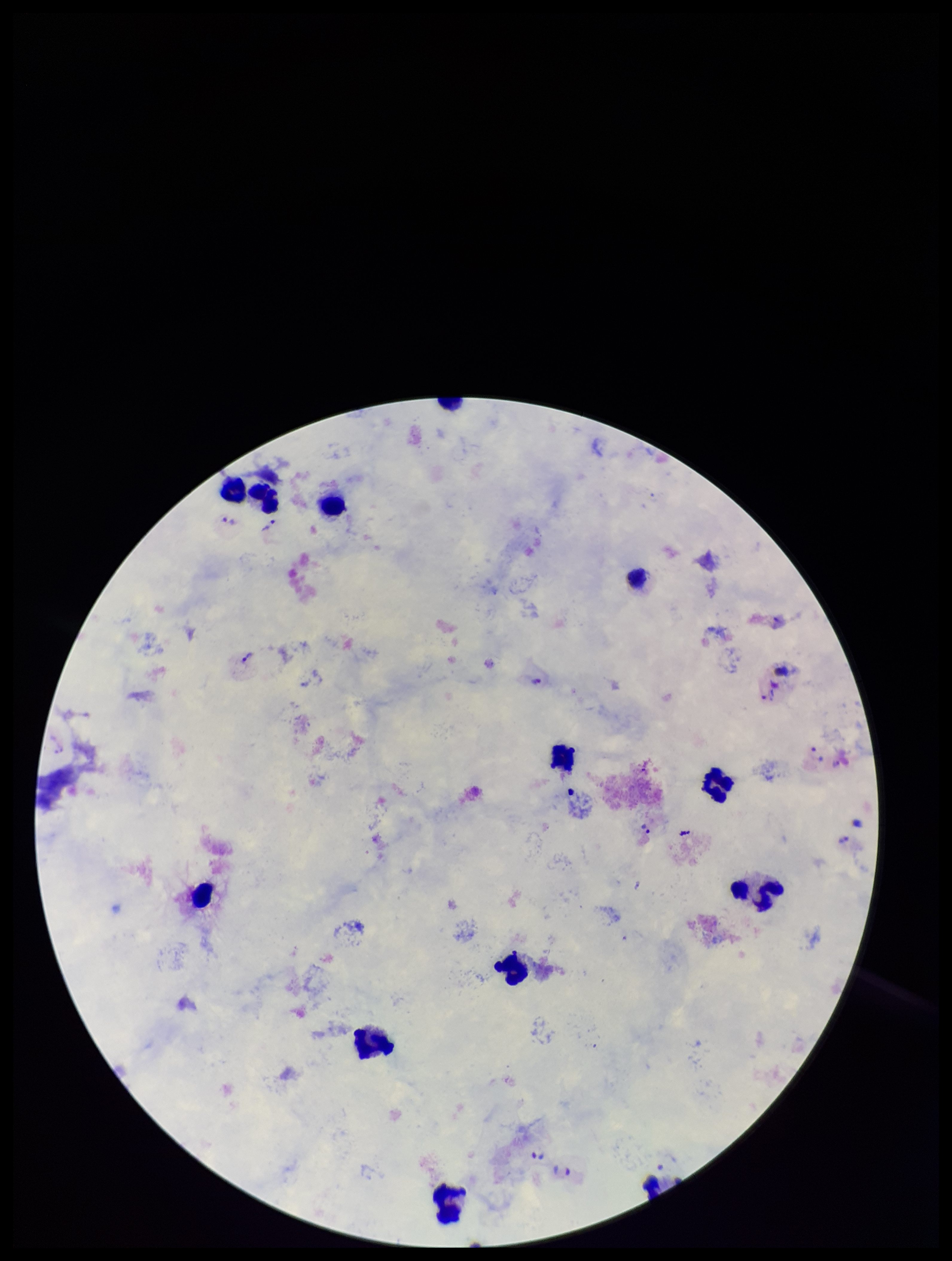
Summary:
  - Preparation: thick smear
  - Plasmodium parasites: identified
  - Patient malaria status: infected
  - Species reported for this patient: Plasmodium vivax
  - Leukocyte count: 13
  - Image size: 952×1261 pixels
  - Field of view: single
  - Capture: smartphone photograph through the microscope eyepiece
  - Parasite count: 8
  - Stain: Giemsa